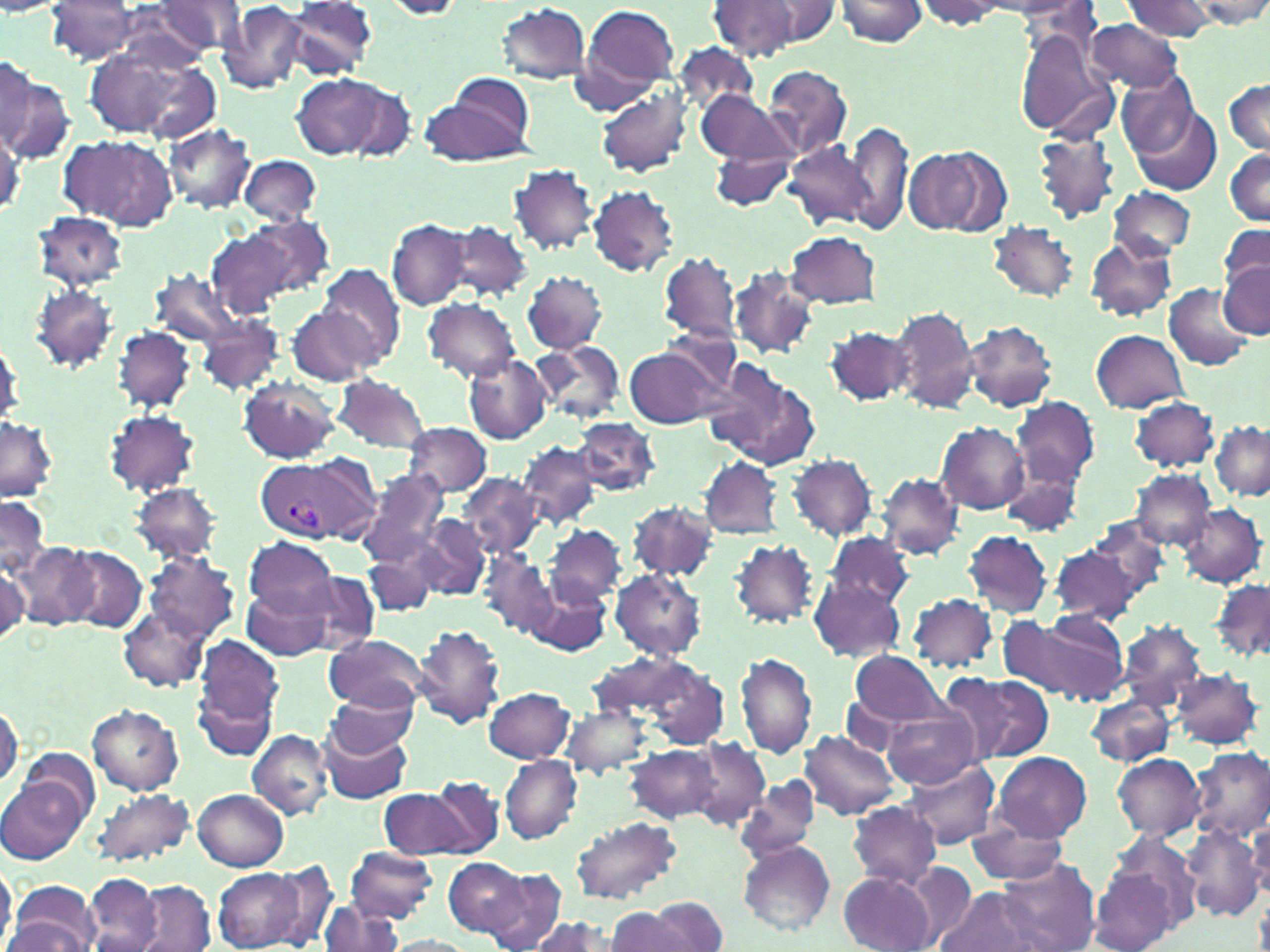
Summary:
  - Coordinate format: approximate bounding boxes as (x1,y1)-(x2,y2) corner pairs in pixels
  - Plasmodium vivax-infected red blood cell locations: (256,457)-(367,545)
  - Uninfected red blood cell locations: (284,0)-(379,79), (753,0)-(843,45), (832,0)-(931,45), (985,0)-(1095,21), (1190,0)-(1270,29), (152,1)-(247,55), (379,1)-(470,19), (709,1)-(802,61), (913,1)-(1016,29), (1125,1)-(1217,41), (44,2)-(144,63), (219,2)-(312,92), (573,3)-(681,108), (496,4)-(593,83), (1086,19)-(1184,94), (1014,30)-(1119,142), (84,43)-(218,141), (674,44)-(760,114), (1,51)-(36,153), (0,63)-(72,165), (762,65)-(852,162), (1117,69)-(1200,158), (431,70)-(538,165), (291,73)-(401,161), (1222,79)-(1270,156), (596,83)-(694,181), (695,90)-(794,170), (1130,106)-(1223,196), (845,120)-(913,235), (162,123)-(256,214), (58,131)-(177,228), (1031,131)-(1121,222), (786,139)-(880,230), (904,147)-(997,236), (1224,147)-(1270,226), (710,150)-(794,207), (238,154)-(322,226), (509,165)-(600,254), (588,186)-(680,276), (1106,186)-(1196,259), (32,212)-(129,292), (208,215)-(330,319), (387,218)-(472,310), (446,218)-(533,303), (987,221)-(1081,302), (1219,223)-(1270,291), (788,230)-(882,310), (1086,236)-(1177,322), (660,250)-(740,345), (1217,261)-(1269,338), (320,263)-(405,367), (728,266)-(820,360), (154,269)-(243,349), (522,271)-(607,355), (1163,283)-(1254,370), (29,284)-(119,370), (424,299)-(520,382), (286,303)-(382,386), (889,306)-(978,415), (195,315)-(284,396), (963,321)-(1057,412), (826,325)-(915,406), (114,326)-(195,413), (1092,329)-(1188,412), (0,334)-(23,430), (528,339)-(627,424), (624,344)-(726,431), (464,354)-(551,444), (700,358)-(819,469), (237,377)-(341,464), (332,377)-(433,452), (1130,396)-(1218,473), (1010,397)-(1099,489), (104,409)-(201,496), (0,414)-(58,503), (573,418)-(659,496), (1211,420)-(1270,499), (403,422)-(492,496), (935,422)-(1029,513), (517,441)-(601,529), (787,454)-(878,542), (700,457)-(783,539), (1000,464)-(1084,538), (357,470)-(449,567), (1131,470)-(1216,551), (877,472)-(964,560), (457,473)-(542,559), (130,482)-(221,564), (0,496)-(50,580), (629,499)-(718,582), (1179,503)-(1266,589), (1083,514)-(1171,605), (411,515)-(489,601), (544,524)-(626,608), (962,530)-(1052,618), (824,531)-(914,610), (244,536)-(337,618), (729,538)-(820,629), (9,541)-(99,629), (1050,542)-(1148,626), (64,546)-(147,632), (363,546)-(440,618), (144,550)-(240,641), (480,552)-(558,638), (0,559)-(29,644), (300,569)-(381,653), (611,569)-(706,660), (524,577)-(607,658), (809,578)-(907,663), (1211,579)-(1270,665), (245,586)-(337,660), (909,592)-(999,674), (119,605)-(212,691), (1017,613)-(1130,705), (1118,623)-(1208,712), (413,625)-(506,729), (327,634)-(428,713), (190,644)-(282,759), (852,649)-(947,728), (736,652)-(816,758), (587,654)-(700,724), (854,654)-(972,779), (630,659)-(730,750), (1169,666)-(1265,750), (954,673)-(1054,762), (484,687)-(575,763), (326,690)-(419,757), (1086,693)-(1177,766), (837,697)-(913,755), (0,702)-(22,790), (563,703)-(655,779), (881,703)-(983,789), (88,706)-(182,795), (317,725)-(412,804), (246,729)-(333,819), (801,729)-(901,819), (688,739)-(768,829), (628,745)-(720,823), (22,747)-(99,826), (1189,748)-(1270,842), (992,751)-(1091,842), (1112,753)-(1204,840), (499,755)-(582,843), (902,759)-(999,849), (0,777)-(85,865), (417,777)-(503,858), (733,778)-(822,863), (91,787)-(194,868), (379,787)-(473,859), (193,789)-(289,870), (847,800)-(942,888), (570,815)-(683,904), (1245,817)-(1270,899), (967,819)-(1069,885), (1183,823)-(1265,921), (737,841)-(835,935), (344,848)-(439,923), (443,856)-(529,937), (995,857)-(1101,952), (1091,858)-(1184,952), (0,860)-(17,949), (904,863)-(977,945), (268,864)-(338,948), (213,868)-(304,951), (479,869)-(566,951), (838,871)-(936,952), (85,874)-(162,950), (136,882)-(214,952), (9,884)-(102,952), (935,885)-(1046,952), (653,896)-(728,951), (318,900)-(405,952), (604,907)-(684,952), (526,916)-(612,952), (3,917)-(95,950), (386,936)-(475,952)
  - Slide-level diagnosis: Plasmodium vivax
  - Stain: May-Grünwald-Giemsa
  - Preparation: thin blood smear
  - Magnification: 1000x
  - Field of view: one of a larger specimen
  - Modality: optical microscopy
  - Image size: 1270×952 pixels